Locate every Plasmodium malariae-infected red blood cell.
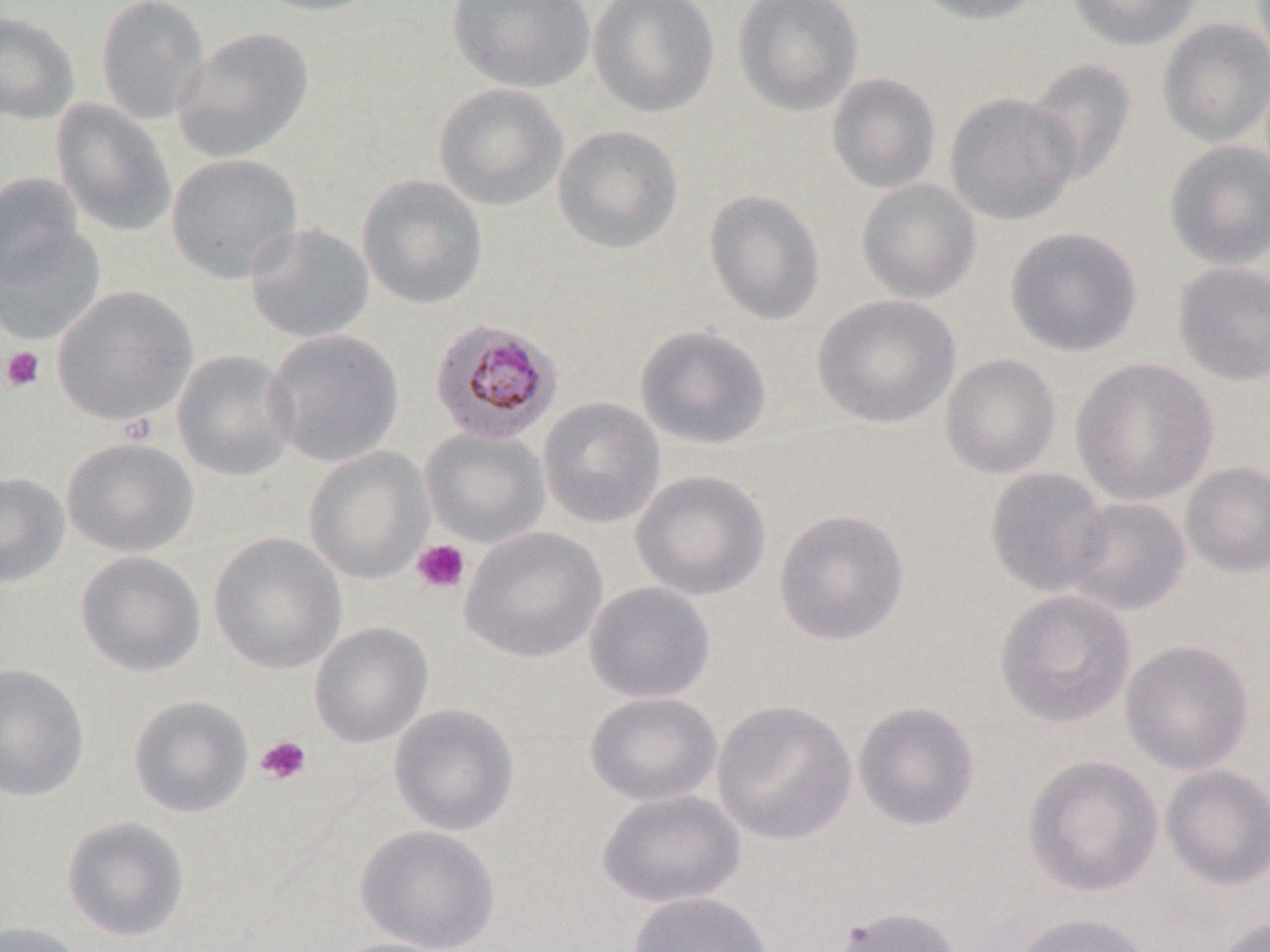

Approximate bounding boxes as (x1,y1)-(x2,y2) corner pairs in pixels.
Plasmodium malariae-infected red blood cells: (429,317)-(564,446).

Platelet locations: (1,346)-(45,392), (117,412)-(158,446), (411,539)-(470,593), (255,735)-(312,785). Uninfected red blood cell locations: (95,0)-(210,125), (250,0)-(384,17), (446,0)-(596,93), (588,0)-(720,118), (731,0)-(865,116), (911,0)-(1047,26), (1066,0)-(1202,51), (0,10)-(80,125), (1157,17)-(1270,148), (172,26)-(314,163), (1025,57)-(1138,187), (826,72)-(942,195), (433,82)-(569,212), (944,91)-(1082,227), (50,98)-(177,239), (552,123)-(685,254), (1163,139)-(1270,270), (165,152)-(304,285), (0,171)-(88,291), (356,173)-(489,310), (855,177)-(982,304), (704,189)-(826,325), (1,212)-(107,345), (244,221)-(375,344), (1005,225)-(1144,357), (1172,261)-(1270,387), (51,285)-(197,426), (812,294)-(962,429), (634,323)-(772,450), (264,329)-(405,468), (172,349)-(299,482), (940,353)-(1062,479), (1070,357)-(1220,506), (538,396)-(666,529), (420,426)-(551,548), (61,437)-(199,558), (304,446)-(434,584), (1180,460)-(1270,578), (983,467)-(1112,598), (630,468)-(772,602), (0,472)-(70,588), (1062,496)-(1191,616), (773,507)-(911,647), (460,526)-(608,664), (208,532)-(348,675), (74,551)-(206,678), (584,580)-(717,704), (994,590)-(1136,729), (308,622)-(433,748), (1119,639)-(1255,776), (0,663)-(90,802), (584,691)-(725,807), (127,695)-(253,819), (712,699)-(857,846), (852,701)-(981,832), (388,704)-(519,836), (1022,755)-(1164,897), (1160,764)-(1270,891), (596,788)-(746,909), (61,816)-(190,943), (355,825)-(501,951), (626,891)-(776,952), (831,906)-(963,952), (1011,912)-(1155,952), (1212,917)-(1269,952), (0,920)-(93,952), (321,937)-(458,952). Slide-level diagnosis: Plasmodium malariae. May-Grünwald-Giemsa-stained preparation. Thin blood smear. One field of a larger specimen. Optical microscopy. Captured at 1000x magnification. Image is 1270×952 pixels.